Assess this cell for malaria.
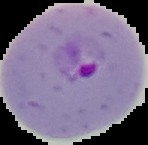

It is parasitized.

The area outside the segmented cell region is set to black. From a thin blood film. Image is 148×145 pixels.